State the preparation type.
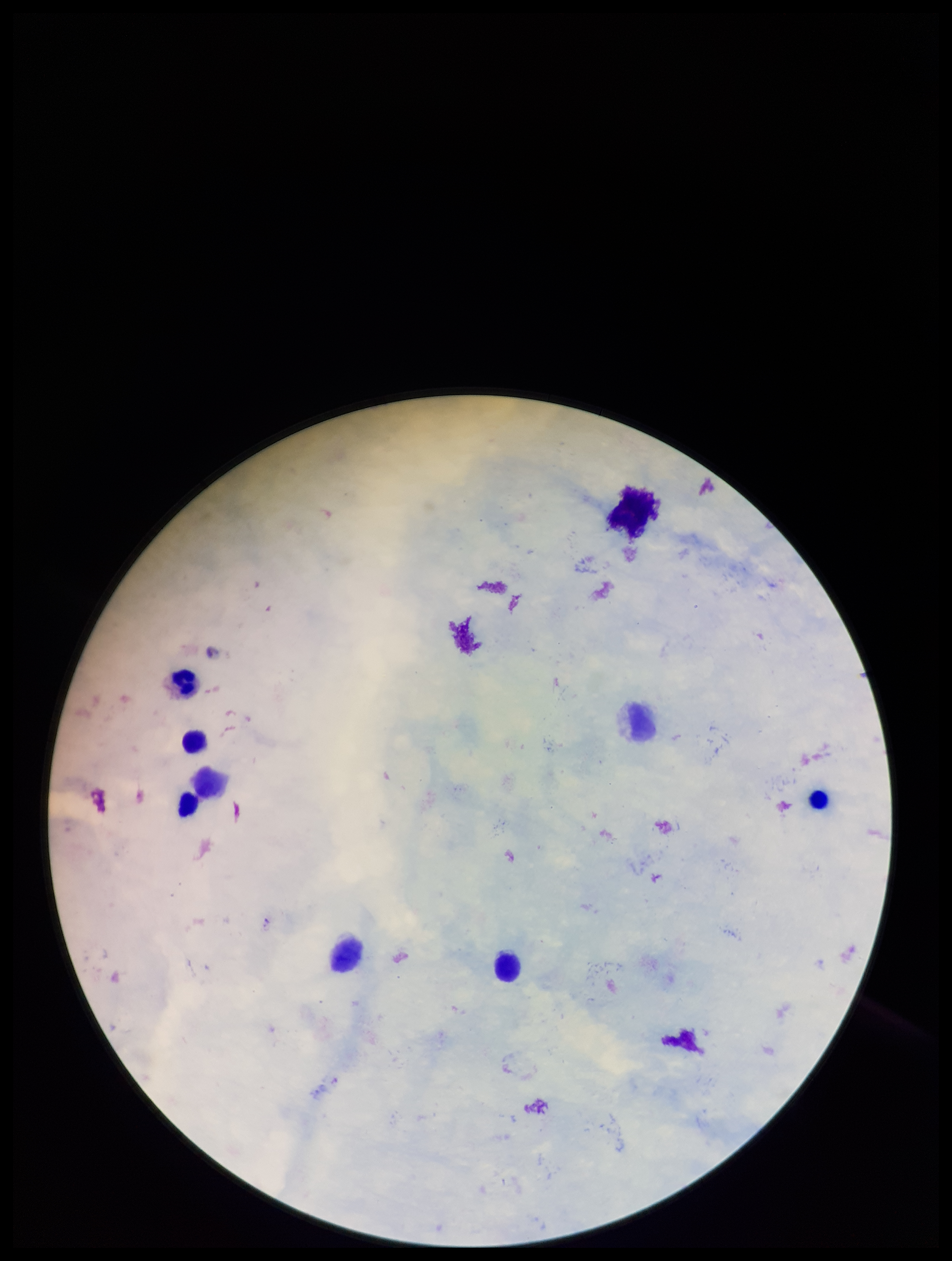
It is a thick blood smear.

Single field of view. Parasite count: 0. Leukocyte count: 5. Photographed through the microscope eyepiece with a smartphone camera. Stained with Giemsa. Plasmodium parasites: none detected. Image is 952×1261 pixels. Patient malaria status: negative.